Assess the morphology of the erythrocytes.
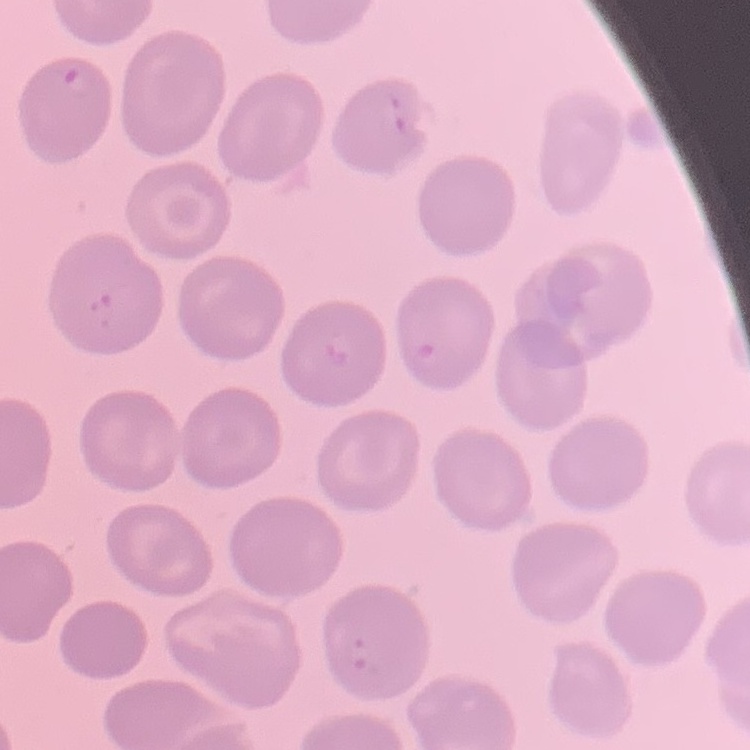
No rouleaux formation.

Summary:
  - Preparation: thin blood film
  - Stain: Field's or Giemsa
  - Image type: square crop of a larger photomicrograph